State which parasite is depicted.
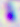
This is Toxoplasma gondii.

Captured at 400x magnification. Photomicrograph.